Assess the morphology of the erythrocytes.
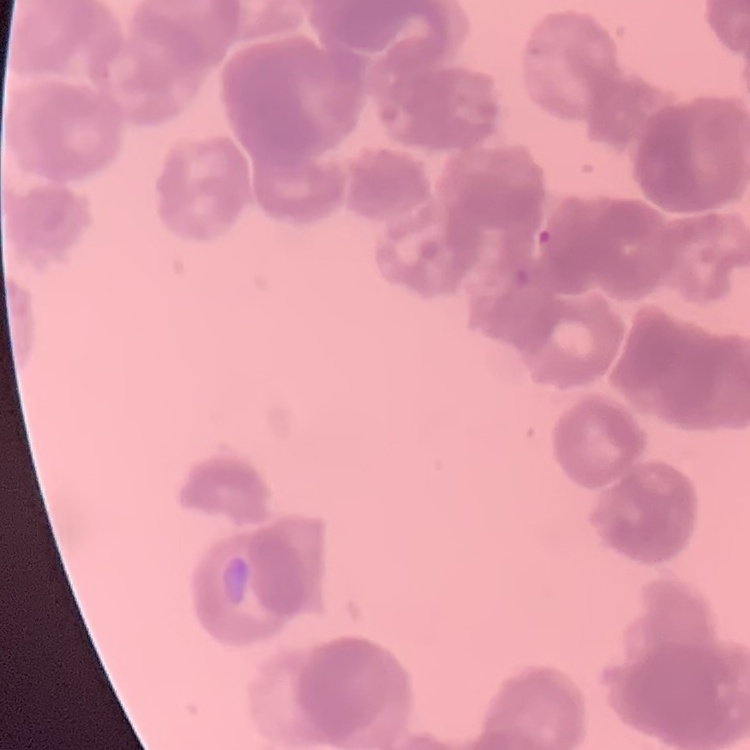
They show rouleaux formation.

One tile cut from a larger photomicrograph. Field's or Giemsa stain. Thin blood smear.